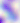 400x magnification. Toxoplasma gondii is seen. Photomicrograph.